Classify this cell by malaria status.
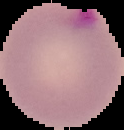

It is parasitized.

image type = cell region segmented out of the field of view; surrounding area masked to black
preparation = thin blood smear
image size = 124×130 pixels